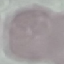
Result: negative for malaria parasites. Acquired by smartphone through the microscope eyepiece. Thin blood film. Cell patch, automatically extracted from a larger field of view and resized to 64 × 64 pixels. Giemsa-stained preparation.